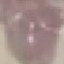

malaria_status: uninfected
image_type: cell patch, automatically extracted from a larger field of view and resized to 64 × 64 pixels
capture: smartphone camera at the microscope eyepiece
preparation: thin blood film
stain: Giemsa